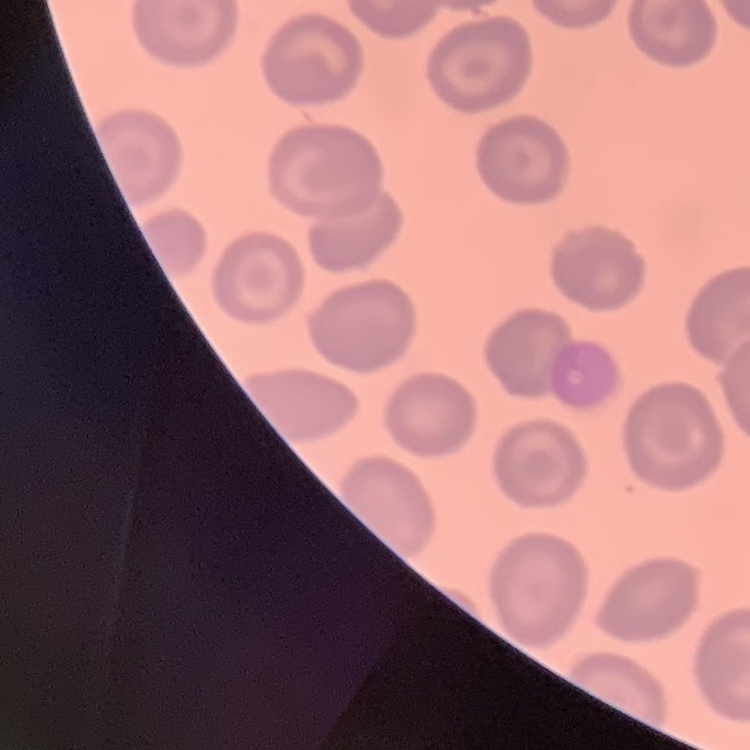
erythrocyte_morphology: no rouleaux formation
stain: Field's or Giemsa
image_type: square crop of a larger photomicrograph
preparation: thin blood film